Locate every blood parasite and identify its species.
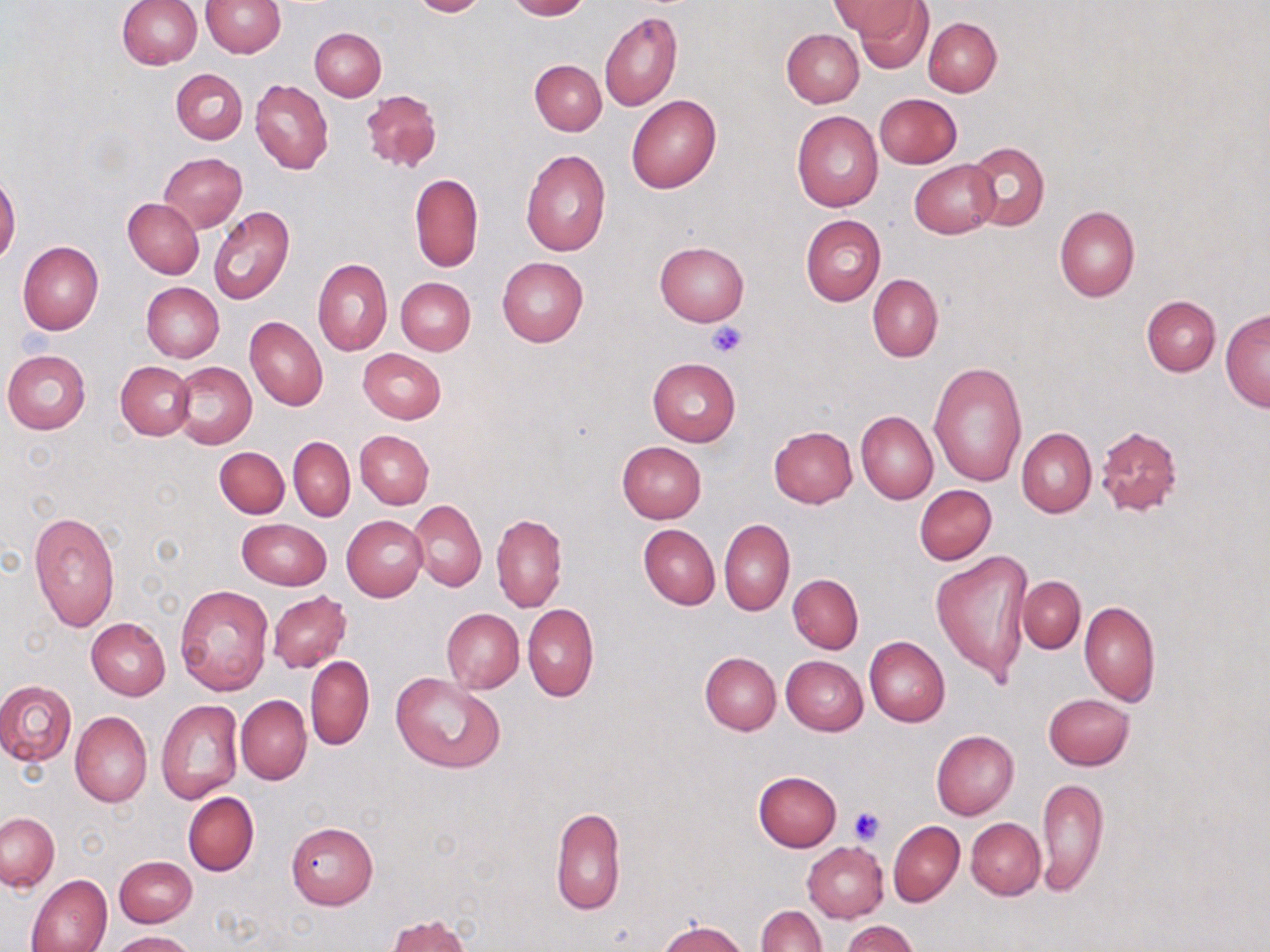

No blood parasites seen.

Approximate bounding boxes as named x1/y1/x2/y2 corners in pixels. Uninfected red blood cell locations: (x1=200, y1=0, x2=285, y2=57), (x1=408, y1=0, x2=489, y2=17), (x1=504, y1=0, x2=589, y2=20), (x1=832, y1=0, x2=919, y2=43), (x1=116, y1=1, x2=201, y2=69), (x1=853, y1=2, x2=933, y2=73), (x1=599, y1=11, x2=682, y2=111), (x1=923, y1=17, x2=1002, y2=96), (x1=309, y1=28, x2=385, y2=100), (x1=781, y1=28, x2=863, y2=107), (x1=529, y1=60, x2=606, y2=136), (x1=172, y1=68, x2=248, y2=144), (x1=250, y1=79, x2=333, y2=175), (x1=361, y1=89, x2=442, y2=174), (x1=875, y1=93, x2=962, y2=168), (x1=626, y1=94, x2=721, y2=193), (x1=791, y1=111, x2=883, y2=212), (x1=966, y1=141, x2=1049, y2=232), (x1=521, y1=150, x2=611, y2=255), (x1=159, y1=153, x2=247, y2=232), (x1=910, y1=159, x2=1000, y2=238), (x1=410, y1=173, x2=482, y2=272), (x1=0, y1=174, x2=21, y2=265), (x1=124, y1=198, x2=204, y2=279), (x1=209, y1=205, x2=295, y2=304), (x1=1054, y1=205, x2=1140, y2=301), (x1=801, y1=214, x2=885, y2=306), (x1=18, y1=241, x2=104, y2=335), (x1=655, y1=241, x2=749, y2=325), (x1=496, y1=257, x2=588, y2=346), (x1=313, y1=258, x2=392, y2=355), (x1=867, y1=274, x2=942, y2=361), (x1=395, y1=277, x2=475, y2=354), (x1=142, y1=281, x2=223, y2=363), (x1=1142, y1=295, x2=1220, y2=376), (x1=1220, y1=310, x2=1269, y2=411), (x1=244, y1=316, x2=328, y2=410), (x1=357, y1=348, x2=445, y2=424), (x1=2, y1=350, x2=91, y2=434), (x1=647, y1=357, x2=739, y2=447), (x1=116, y1=361, x2=194, y2=440), (x1=170, y1=361, x2=256, y2=448), (x1=928, y1=362, x2=1028, y2=486), (x1=856, y1=411, x2=938, y2=504), (x1=768, y1=426, x2=858, y2=508), (x1=1095, y1=426, x2=1181, y2=517), (x1=1017, y1=427, x2=1096, y2=518), (x1=355, y1=430, x2=433, y2=508), (x1=289, y1=436, x2=354, y2=521), (x1=617, y1=441, x2=707, y2=523), (x1=214, y1=447, x2=289, y2=518), (x1=915, y1=484, x2=997, y2=565), (x1=410, y1=499, x2=486, y2=591), (x1=29, y1=509, x2=120, y2=633), (x1=492, y1=514, x2=567, y2=613), (x1=342, y1=515, x2=428, y2=601), (x1=237, y1=518, x2=331, y2=590), (x1=719, y1=519, x2=794, y2=616), (x1=638, y1=524, x2=719, y2=609), (x1=931, y1=547, x2=1034, y2=688), (x1=788, y1=574, x2=863, y2=653), (x1=1017, y1=576, x2=1085, y2=653), (x1=175, y1=584, x2=273, y2=695), (x1=267, y1=591, x2=352, y2=673), (x1=1079, y1=601, x2=1160, y2=705), (x1=522, y1=604, x2=598, y2=702), (x1=441, y1=608, x2=523, y2=693), (x1=86, y1=618, x2=171, y2=699), (x1=864, y1=636, x2=950, y2=727), (x1=700, y1=652, x2=780, y2=735), (x1=305, y1=656, x2=374, y2=751), (x1=780, y1=656, x2=868, y2=735), (x1=391, y1=672, x2=507, y2=774), (x1=0, y1=680, x2=77, y2=766), (x1=1043, y1=693, x2=1135, y2=771), (x1=235, y1=695, x2=312, y2=784), (x1=156, y1=700, x2=243, y2=803), (x1=70, y1=711, x2=152, y2=807), (x1=931, y1=730, x2=1018, y2=820), (x1=753, y1=771, x2=842, y2=851), (x1=1036, y1=775, x2=1108, y2=894), (x1=183, y1=792, x2=258, y2=877), (x1=549, y1=806, x2=625, y2=915), (x1=1, y1=812, x2=59, y2=891), (x1=966, y1=818, x2=1045, y2=900), (x1=887, y1=820, x2=964, y2=906), (x1=286, y1=821, x2=379, y2=909), (x1=803, y1=842, x2=888, y2=922), (x1=114, y1=856, x2=196, y2=928), (x1=26, y1=874, x2=112, y2=952), (x1=755, y1=905, x2=826, y2=952), (x1=386, y1=914, x2=470, y2=952), (x1=657, y1=919, x2=751, y2=952), (x1=842, y1=920, x2=919, y2=952), (x1=110, y1=930, x2=195, y2=951). Platelet locations: (x1=706, y1=322, x2=748, y2=359), (x1=850, y1=805, x2=885, y2=843). Slide-level diagnosis: negative for blood parasites. 1000x magnification. Image is 1270×952 pixels. Optical microscopy. May-Grünwald-Giemsa stain. One field of a larger specimen. Thin blood smear.